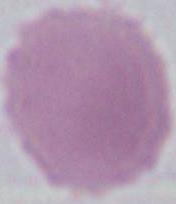

{
  "identification": "red blood cell",
  "modality": "photomicrograph",
  "magnification": "1000x"
}